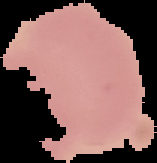
{
  "image_size": "157×163 pixels",
  "image_type": "segmented cell region on a black background",
  "preparation": "thin blood smear",
  "malaria_status": "uninfected"
}